Identify the cell.
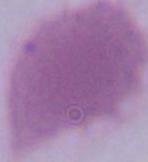

An erythrocyte.

Captured at 1000x magnification. Micrograph.